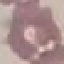
malaria status = uninfected
stain = Giemsa
image type = cell patch, automatically extracted from a larger field of view and resized to 64 × 64 pixels
capture = smartphone through the microscope eyepiece
preparation = thin smear